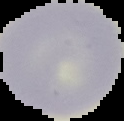
Summary:
  - Image size: 124×121 pixels
  - Preparation: thin blood smear
  - Image type: segmented cell region with the area outside set to black
  - Result: negative for Plasmodium parasites